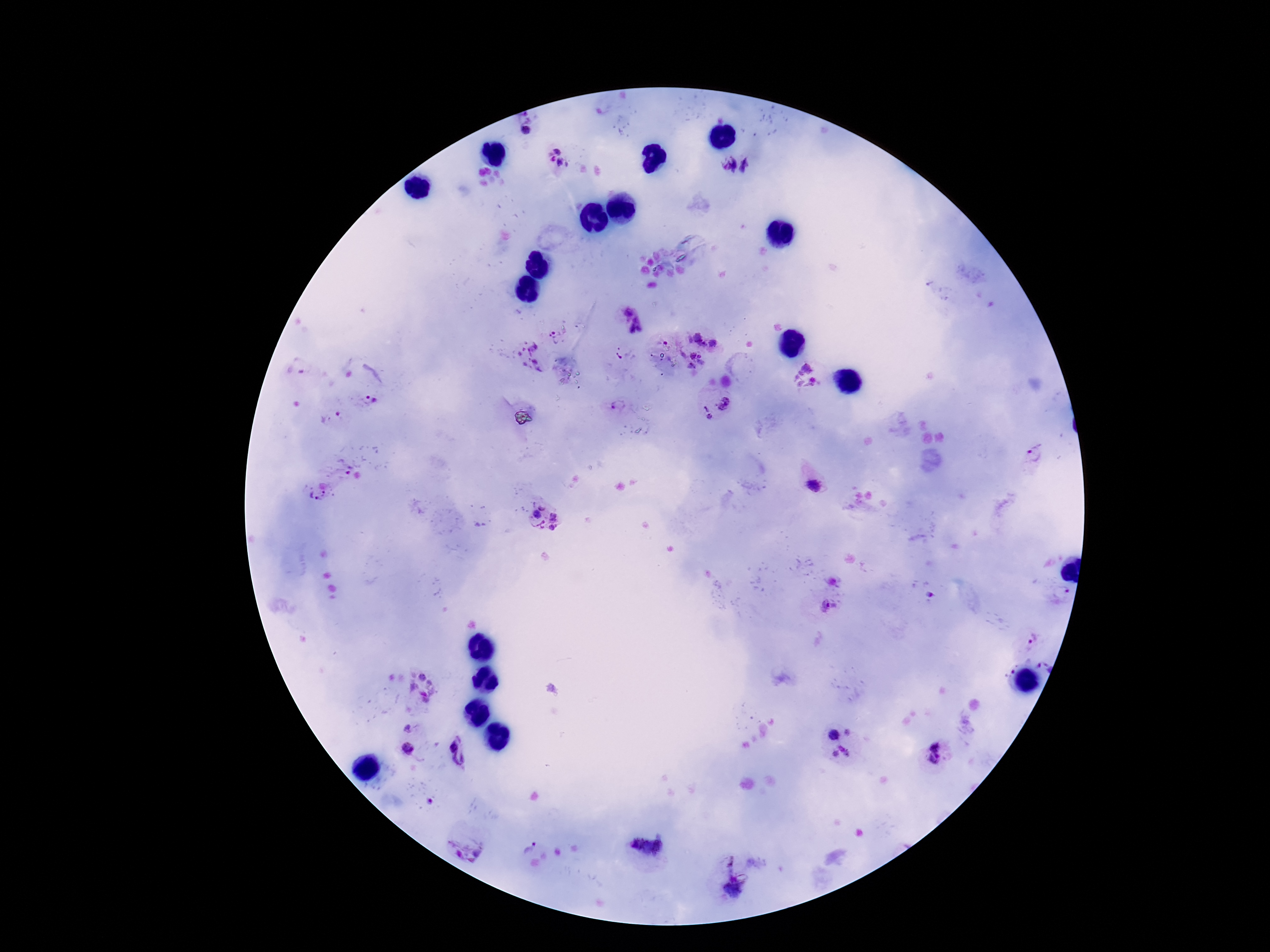

Approximate object centers, in pixels from the top-left corner. Plasmodium parasite locations: (x=526, y=131), (x=557, y=151), (x=552, y=159), (x=563, y=163), (x=727, y=165), (x=747, y=166), (x=626, y=312), (x=637, y=318), (x=630, y=328), (x=639, y=328), (x=552, y=333), (x=696, y=336), (x=690, y=340), (x=712, y=343), (x=702, y=345), (x=692, y=355), (x=700, y=356), (x=692, y=366), (x=805, y=377), (x=368, y=400), (x=724, y=403), (x=618, y=406), (x=706, y=408), (x=340, y=416), (x=710, y=416), (x=1034, y=453), (x=346, y=470), (x=817, y=487), (x=319, y=494), (x=543, y=505), (x=536, y=514), (x=554, y=517), (x=537, y=526), (x=553, y=527), (x=1061, y=593), (x=930, y=597), (x=828, y=607), (x=1033, y=639), (x=422, y=677), (x=832, y=735), (x=460, y=748), (x=408, y=749), (x=841, y=753), (x=934, y=754), (x=648, y=840), (x=529, y=848), (x=733, y=891). Giemsa-stained preparation. 100x magnification. Patient malaria status: positive. Image is 1270×952 pixels. Smartphone photograph taken through the microscope eyepiece. Thick blood film. One field from this slide.